Classify this cell by malaria status.
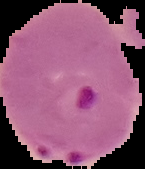
It is parasitized.

image_size: 145×169 pixels
image_type: cell region segmented out of the field of view; surrounding area masked to black
preparation: thin blood film